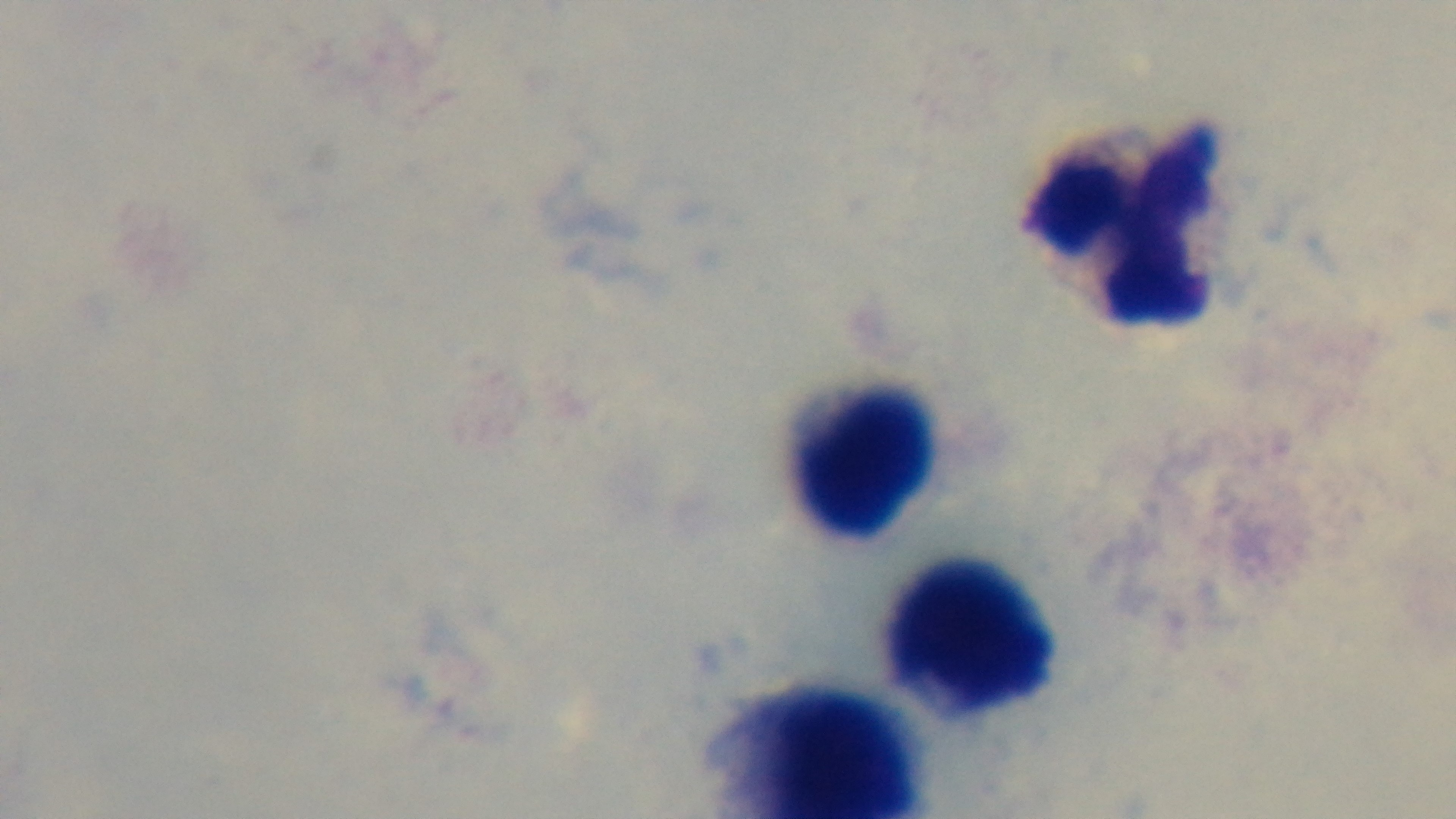
stain = Giemsa
field of view = single
modality = light microscopy
objective = 100x oil immersion
capture = mounted 4K digital camera
malaria status = negative
preparation = thick blood film